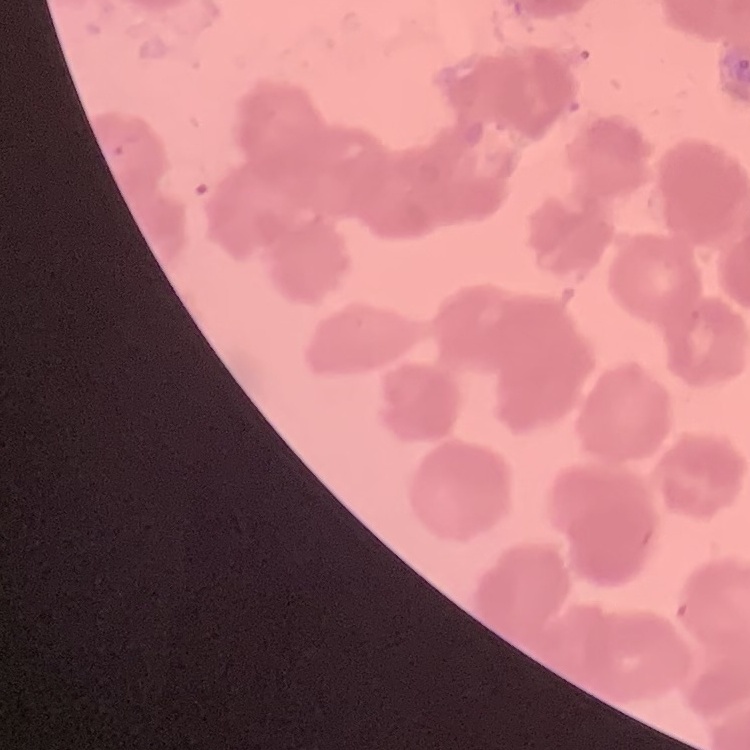

The red blood cells show rouleaux formation. Thin peripheral smear. Square crop of a larger photomicrograph. Stained with either Field's or Giemsa.